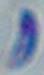
Summary:
  - Magnification: 1000x
  - Modality: photomicrograph
  - Identification: Toxoplasma gondii